Name the cell type shown.
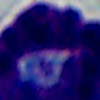
This is a leukocyte.

1000x magnification. Micrograph.